Report the malaria status of this cell.
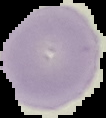

Uninfected.

image_type: cell region segmented out of the field of view; surrounding area masked to black
image_size: 106×118 pixels
preparation: thin blood smear